Describe the morphology of the red blood cells.
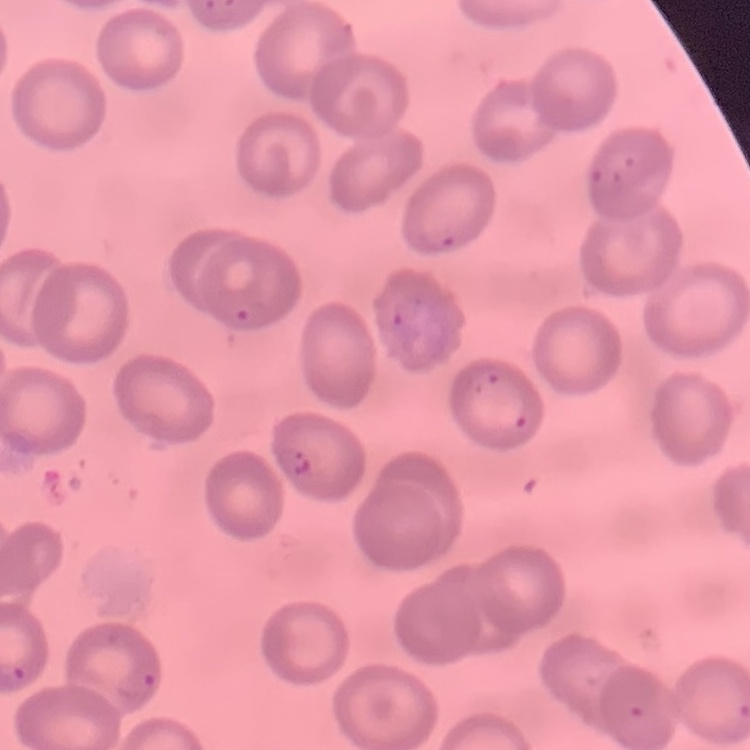

They show no rouleaux formation.

{
  "preparation": "thin blood film",
  "stain": "Field's or Giemsa",
  "image_type": "one tile cut from a larger photomicrograph"
}